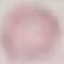

Malaria status: uninfected. Giemsa stain. Cell patch, automatically extracted from a larger field of view and resized to 64 × 64 pixels. Photographed with a smartphone camera at the microscope eyepiece. Thin blood smear.